Locate every blood parasite and identify its species.
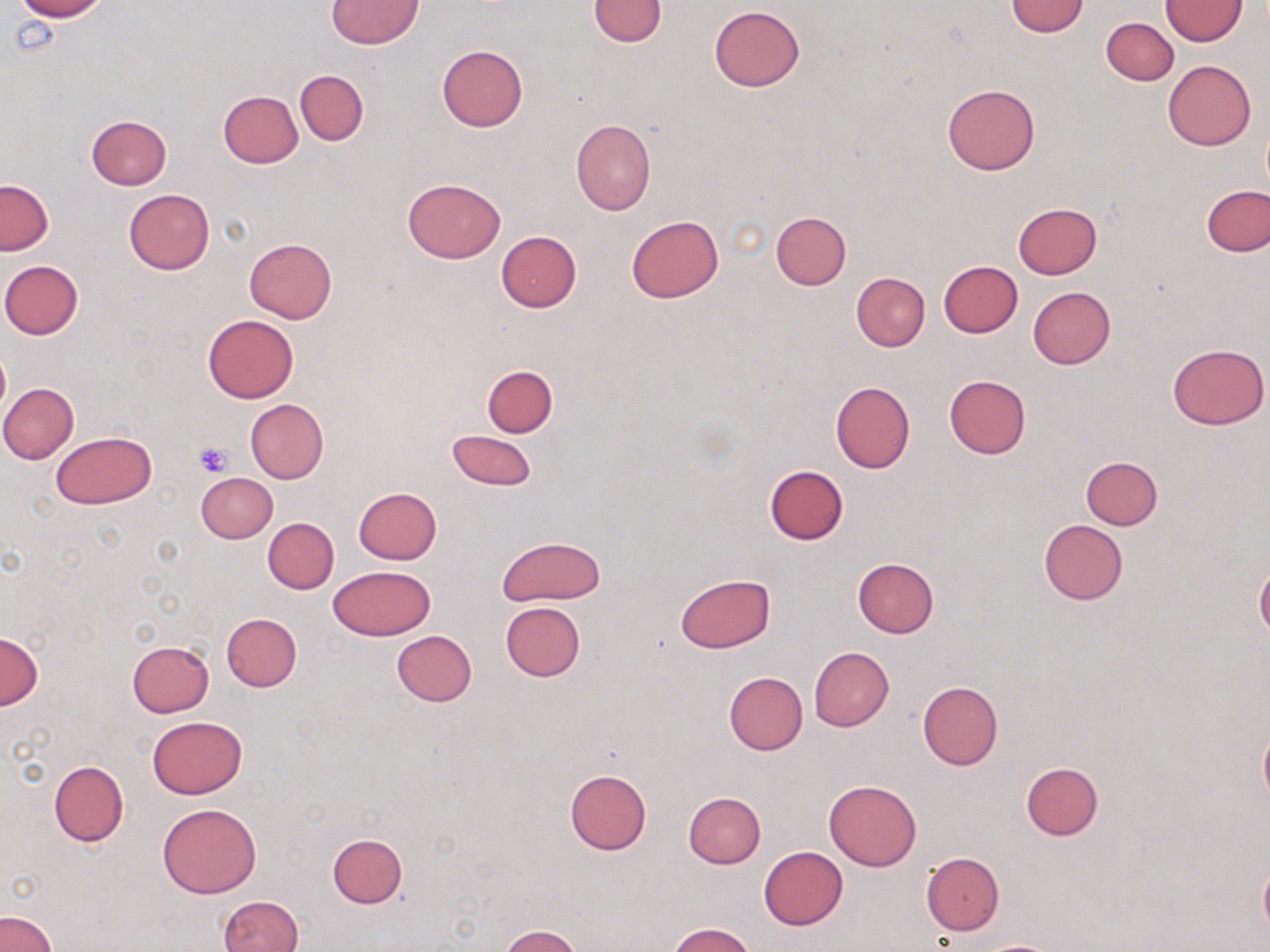

No blood parasites observed.

Approximate bounding boxes as [x1, y1, x2, y2] in pixels. Uninfected red blood cell locations: [14, 0, 107, 21], [326, 0, 422, 49], [588, 0, 668, 46], [1005, 1, 1088, 36], [1161, 1, 1246, 45], [709, 5, 805, 90], [1101, 18, 1178, 85], [436, 45, 528, 132], [1164, 60, 1255, 150], [295, 69, 369, 144], [942, 84, 1040, 176], [217, 90, 303, 167], [87, 116, 172, 190], [571, 119, 656, 215], [403, 178, 506, 262], [1, 180, 53, 255], [1203, 185, 1269, 256], [123, 188, 214, 275], [1013, 202, 1101, 278], [771, 211, 851, 289], [626, 214, 724, 304], [496, 232, 581, 311], [244, 239, 337, 323], [1, 260, 84, 340], [939, 260, 1022, 337], [852, 272, 930, 351], [1028, 286, 1115, 369], [202, 314, 299, 403], [1167, 342, 1268, 430], [0, 347, 10, 421], [482, 365, 557, 437], [944, 374, 1031, 460], [829, 381, 915, 472], [0, 383, 78, 464], [245, 399, 329, 484], [447, 429, 537, 491], [51, 431, 156, 509], [1080, 455, 1163, 529], [764, 464, 848, 545], [197, 471, 278, 543], [353, 487, 442, 564], [263, 516, 339, 594], [1038, 519, 1127, 604], [497, 535, 605, 605], [851, 557, 939, 638], [1255, 563, 1270, 641], [328, 565, 436, 640], [675, 573, 775, 653], [500, 602, 585, 681], [221, 613, 302, 691], [0, 631, 41, 711], [390, 631, 476, 707], [126, 640, 214, 716], [809, 647, 893, 730], [724, 671, 807, 755], [916, 681, 1003, 770], [147, 715, 247, 799], [1258, 716, 1270, 812], [49, 760, 129, 847], [1020, 762, 1102, 840], [565, 769, 651, 855], [824, 780, 921, 870], [683, 791, 766, 869], [157, 804, 261, 898], [328, 833, 407, 908], [759, 846, 847, 929], [920, 852, 1005, 935], [1258, 855, 1270, 940], [218, 895, 303, 952], [0, 910, 57, 952], [666, 923, 756, 952], [500, 925, 581, 952], [971, 938, 1065, 952]. Platelet locations: [195, 442, 231, 477]. Slide-level diagnosis: negative for blood parasites. One field of a larger specimen. Optical microscopy. Captured at 1000x magnification. Image is 1270×952 pixels. May-Grünwald-Giemsa-stained preparation. Thin blood smear.